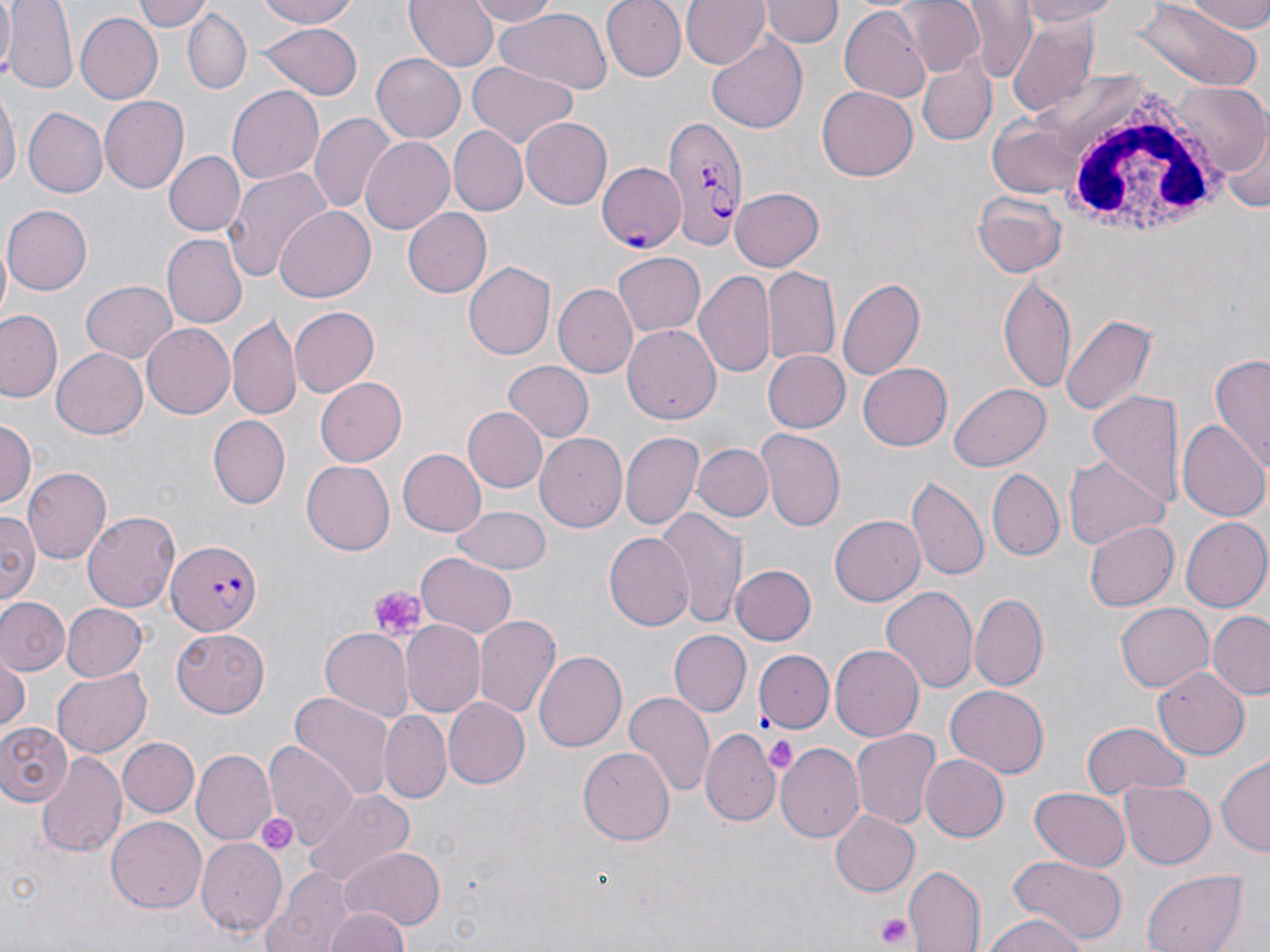

Approximate bounding boxes as [x1, y1, x2, y2] in pixels. Uninfected red blood cell locations: [0, 0, 12, 74], [6, 0, 79, 94], [133, 0, 211, 33], [256, 0, 363, 28], [406, 0, 499, 72], [466, 0, 560, 25], [599, 0, 686, 81], [680, 0, 768, 69], [764, 0, 839, 49], [903, 0, 987, 76], [963, 0, 1034, 83], [1016, 0, 1131, 26], [1183, 0, 1270, 33], [1131, 1, 1263, 89], [837, 6, 931, 104], [494, 8, 612, 92], [183, 9, 251, 94], [73, 12, 162, 105], [1006, 19, 1099, 117], [258, 22, 360, 99], [707, 35, 807, 134], [919, 52, 995, 148], [372, 54, 465, 143], [466, 63, 578, 147], [1174, 83, 1267, 172], [228, 85, 324, 186], [0, 86, 18, 196], [817, 86, 917, 182], [99, 94, 189, 194], [26, 107, 110, 197], [310, 114, 396, 215], [521, 117, 612, 210], [448, 125, 527, 215], [1219, 126, 1269, 215], [360, 137, 455, 237], [165, 151, 244, 234], [223, 168, 332, 284], [729, 187, 824, 272], [971, 192, 1068, 279], [0, 204, 90, 295], [275, 205, 376, 299], [403, 208, 492, 298], [162, 234, 248, 328], [612, 253, 705, 337], [465, 261, 558, 361], [762, 267, 840, 364], [696, 269, 776, 381], [836, 275, 927, 383], [999, 275, 1077, 391], [82, 280, 179, 364], [553, 283, 637, 379], [290, 305, 380, 396], [2, 310, 64, 403], [1060, 311, 1158, 416], [226, 312, 301, 418], [141, 321, 237, 418], [623, 324, 721, 427], [51, 347, 148, 439], [760, 350, 849, 433], [1209, 355, 1269, 469], [502, 361, 593, 441], [859, 362, 953, 450], [315, 378, 406, 466], [949, 384, 1050, 471], [1087, 389, 1182, 513], [463, 407, 546, 490], [207, 414, 289, 507], [0, 418, 36, 512], [1178, 419, 1268, 524], [757, 427, 845, 530], [621, 431, 703, 529], [535, 433, 627, 531], [694, 443, 772, 522], [398, 449, 485, 537], [1062, 454, 1170, 552], [302, 459, 395, 555], [23, 466, 113, 561], [987, 468, 1065, 561], [907, 475, 989, 581], [452, 507, 551, 574], [657, 509, 747, 628], [83, 510, 180, 613], [0, 511, 41, 610], [830, 515, 926, 606], [1180, 517, 1269, 613], [1086, 520, 1178, 611], [604, 532, 694, 630], [418, 552, 517, 636], [728, 564, 814, 646], [880, 585, 978, 693], [970, 592, 1047, 690], [1, 595, 69, 675], [1116, 602, 1212, 692], [61, 603, 147, 681], [1208, 613, 1270, 698], [474, 614, 560, 718], [399, 622, 484, 717], [320, 627, 416, 718], [172, 628, 271, 715], [670, 631, 750, 715], [831, 645, 923, 742], [535, 650, 626, 750], [756, 650, 832, 734], [0, 652, 29, 734], [1153, 666, 1249, 757], [52, 668, 151, 757], [946, 686, 1049, 777], [624, 691, 714, 798], [288, 692, 395, 801], [442, 698, 529, 789], [382, 711, 451, 801], [0, 718, 76, 805], [1080, 720, 1192, 798], [851, 727, 940, 830], [701, 728, 780, 825], [120, 737, 198, 817], [774, 740, 863, 839], [265, 742, 357, 838], [580, 745, 675, 844], [193, 749, 276, 843], [38, 753, 126, 859], [1217, 754, 1270, 855], [921, 756, 1008, 842], [1118, 779, 1215, 870], [1028, 788, 1133, 872], [302, 791, 415, 887], [829, 810, 919, 896], [106, 815, 207, 913], [197, 838, 287, 935], [338, 848, 445, 927], [1008, 855, 1127, 944], [906, 865, 986, 951], [263, 868, 354, 952], [1143, 869, 1246, 952], [323, 907, 411, 952], [977, 913, 1094, 952]. White blood cell locations: [1040, 79, 1226, 242]. Platelet locations: [367, 586, 425, 639], [765, 737, 797, 774], [252, 811, 297, 854], [874, 910, 917, 952]. Plasmodium falciparum-infected red blood cell locations: [659, 114, 748, 249], [591, 158, 684, 256], [166, 537, 260, 634]. Slide-level diagnosis: Plasmodium falciparum. 1000x magnification. Image is 1270×952 pixels. Light microscopy. May-Grünwald-Giemsa-stained preparation. Thin blood smear. One field of a larger specimen.